Identify the parasite.
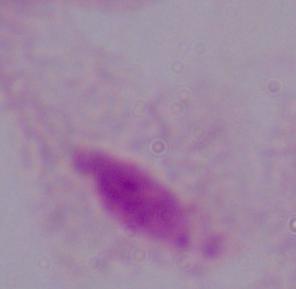

A trichomonad.

Micrograph. 1000x magnification.